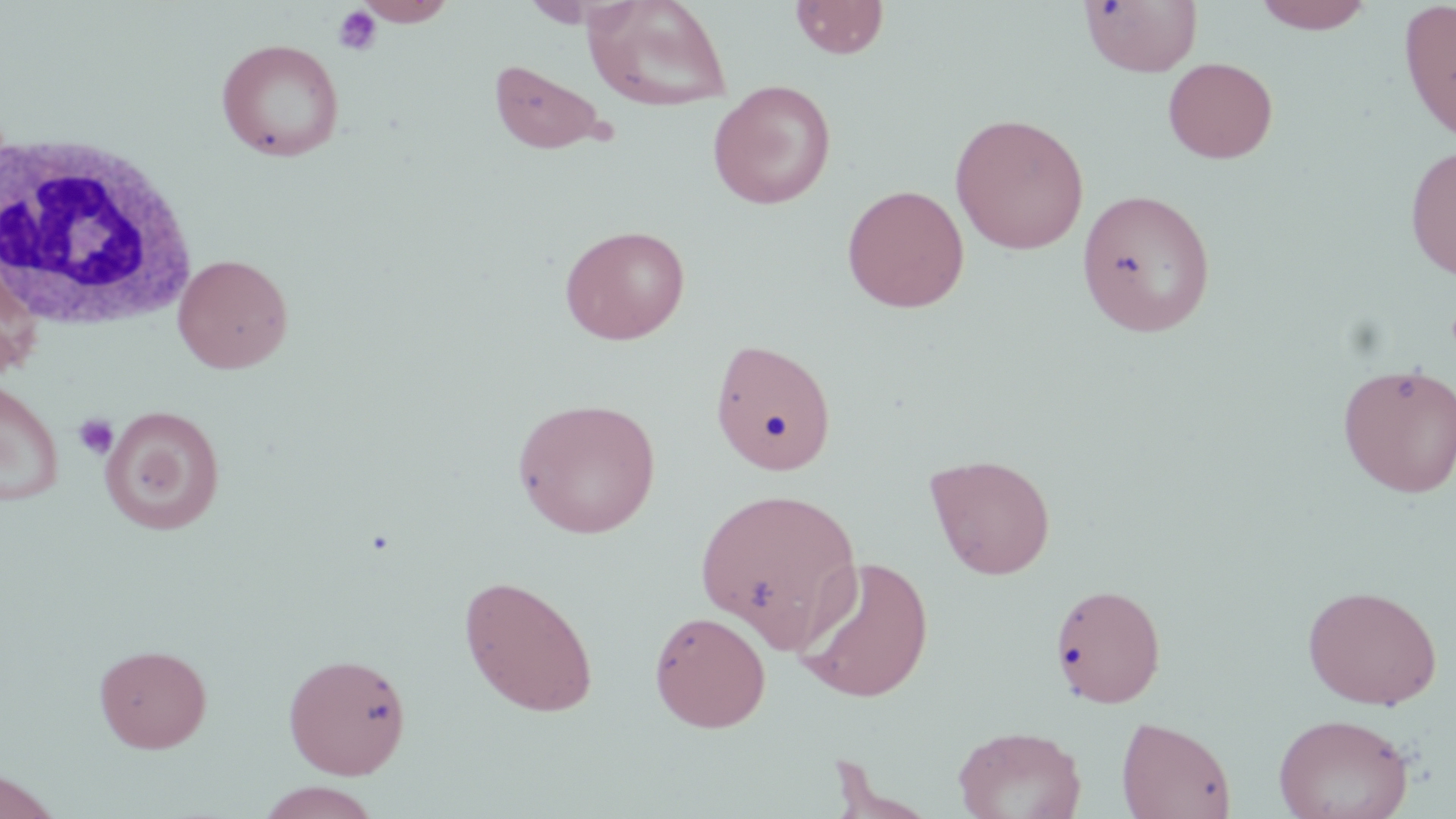 Approximate bounding boxes as named x1/y1/x2/y2 corners in pixels. White blood cell locations: (x1=2, y1=130, x2=199, y2=331). Platelet locations: (x1=332, y1=5, x2=382, y2=56), (x1=73, y1=413, x2=118, y2=460). Uninfected red blood cell locations: (x1=355, y1=0, x2=457, y2=26), (x1=583, y1=0, x2=733, y2=112), (x1=790, y1=0, x2=890, y2=60), (x1=1079, y1=0, x2=1202, y2=77), (x1=1251, y1=0, x2=1376, y2=35), (x1=1397, y1=0, x2=1456, y2=145), (x1=216, y1=38, x2=345, y2=161), (x1=1163, y1=57, x2=1278, y2=164), (x1=487, y1=58, x2=610, y2=155), (x1=707, y1=80, x2=837, y2=209), (x1=950, y1=112, x2=1090, y2=254), (x1=1404, y1=143, x2=1456, y2=280), (x1=841, y1=184, x2=969, y2=313), (x1=1076, y1=188, x2=1217, y2=338), (x1=559, y1=225, x2=691, y2=345), (x1=173, y1=253, x2=293, y2=374), (x1=709, y1=338, x2=837, y2=476), (x1=1337, y1=363, x2=1455, y2=497), (x1=0, y1=378, x2=64, y2=506), (x1=512, y1=397, x2=661, y2=538), (x1=101, y1=405, x2=226, y2=535), (x1=925, y1=453, x2=1056, y2=580), (x1=695, y1=485, x2=862, y2=649), (x1=794, y1=555, x2=935, y2=703), (x1=458, y1=574, x2=599, y2=717), (x1=1050, y1=582, x2=1167, y2=709), (x1=1303, y1=584, x2=1442, y2=709), (x1=649, y1=609, x2=771, y2=733), (x1=94, y1=643, x2=212, y2=753), (x1=282, y1=652, x2=412, y2=779), (x1=1273, y1=713, x2=1414, y2=819), (x1=1116, y1=715, x2=1235, y2=819), (x1=952, y1=725, x2=1086, y2=819), (x1=0, y1=768, x2=62, y2=819), (x1=255, y1=782, x2=385, y2=818). Slide-level diagnosis: no evidence of blood parasites. May-Grünwald-Giemsa-stained preparation. Image is 1456×819 pixels. 1000x magnification. Optical microscopy. Single field of view. Thin blood smear.